Assess this cell for malaria.
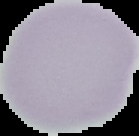

Uninfected.

From a thin blood film. Image is 139×136 pixels. The area outside the segmented cell region is set to black.